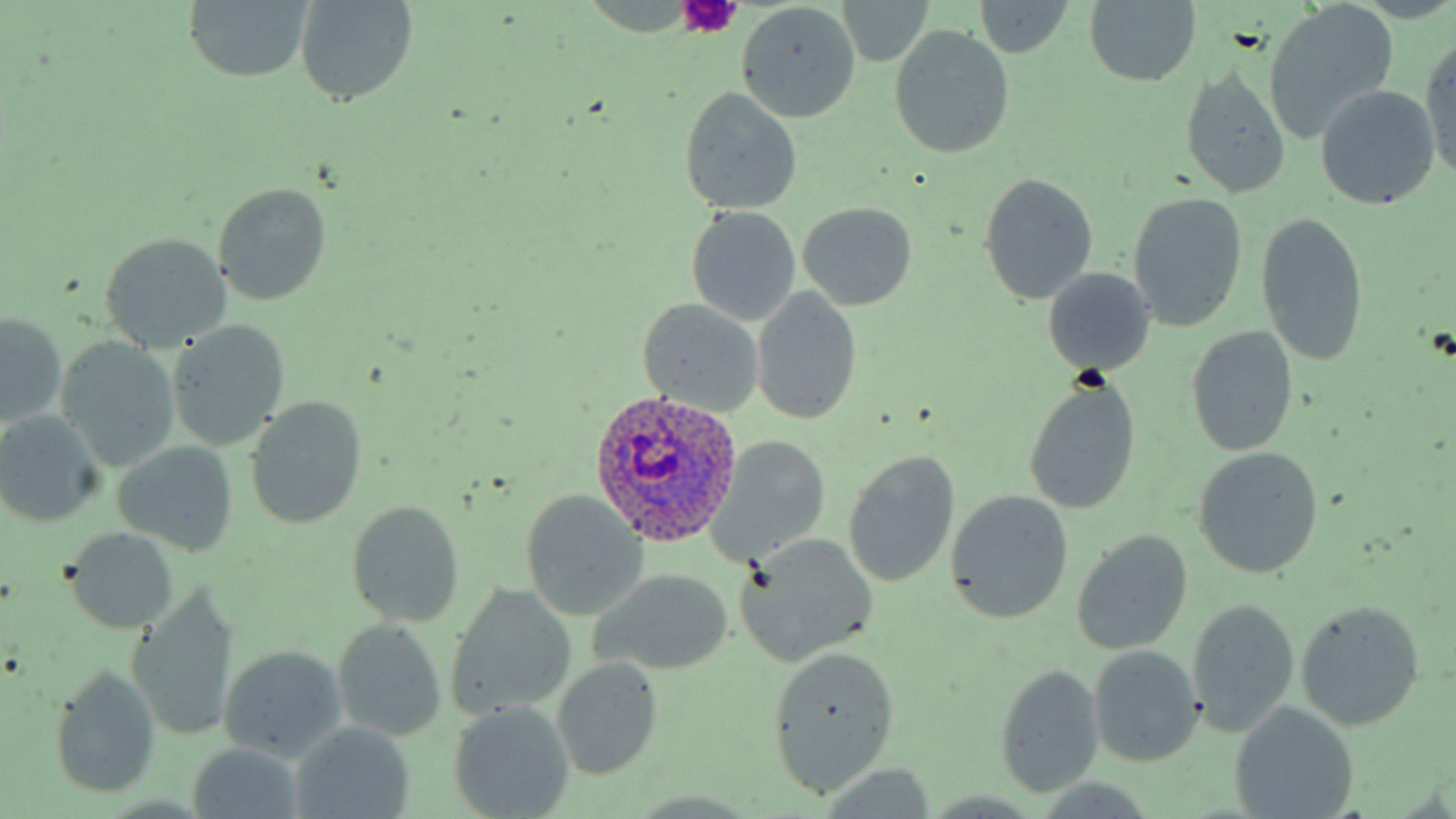 Approximate bounding boxes as (x1,y1)-(x2,y2) corner pairs in pixels. Plasmodium ovale-infected red blood cell locations: (587,388)-(743,545). Uninfected red blood cell locations: (181,0)-(315,84), (294,0)-(420,108), (971,0)-(1073,58), (1083,0)-(1203,88), (836,2)-(936,66), (1264,2)-(1401,143), (736,3)-(862,123), (888,24)-(1014,160), (1419,35)-(1456,183), (1178,66)-(1292,199), (1313,84)-(1442,210), (677,87)-(804,216), (978,172)-(1099,305), (212,181)-(334,306), (1126,192)-(1248,333), (797,201)-(919,310), (685,206)-(802,326), (1255,212)-(1370,369), (97,233)-(233,351), (1041,267)-(1156,377), (751,287)-(863,425), (636,298)-(766,416), (1,311)-(68,428), (164,321)-(291,451), (1184,326)-(1299,457), (55,336)-(181,471), (1023,376)-(1142,516), (242,396)-(370,530), (0,410)-(107,528), (714,435)-(832,561), (111,439)-(241,557), (1191,447)-(1325,579), (842,450)-(961,590), (944,488)-(1075,626), (519,490)-(651,621), (344,499)-(466,628), (62,526)-(180,633), (1071,529)-(1193,654), (735,533)-(879,667), (587,568)-(736,677), (446,584)-(578,720), (126,590)-(242,741), (1186,597)-(1299,738), (1295,599)-(1427,731), (331,618)-(449,742), (763,643)-(900,798), (217,644)-(349,763), (1087,644)-(1205,767), (551,656)-(665,781), (49,663)-(162,801), (993,664)-(1105,799), (447,700)-(575,819), (1230,702)-(1360,818), (289,723)-(416,818), (185,742)-(309,818). Platelet locations: (676,0)-(744,35). Slide-level diagnosis: Plasmodium ovale. Image is 1456×819 pixels. May-Grünwald-Giemsa-stained preparation. Thin blood film. One field of a larger specimen. Captured at 1000x magnification. Light microscopy.